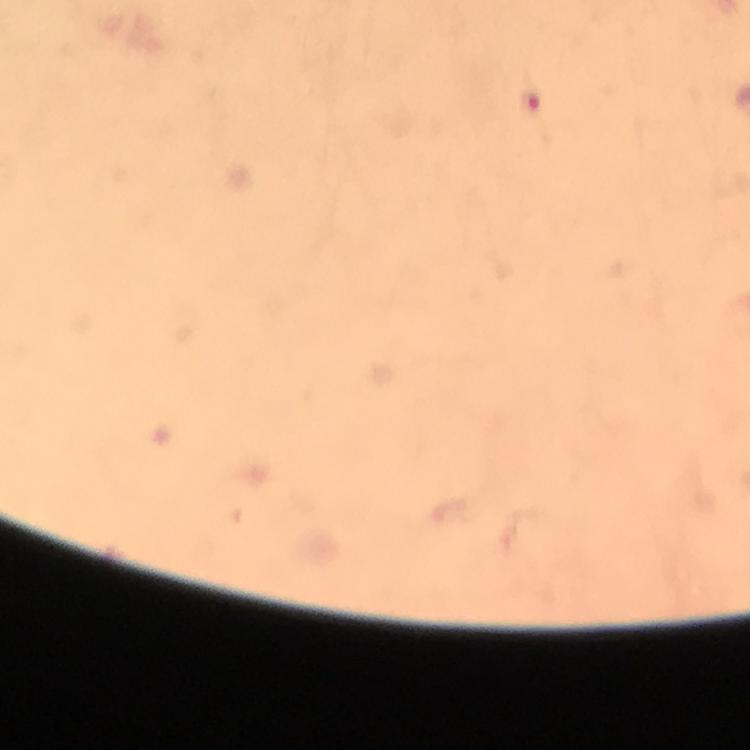

Approximate centers as (x, y) in pixels.
Summary:
  - Malaria parasite locations: (531, 107)
  - Capture: smartphone camera through the microscope
  - Image size: 750×750 pixels
  - Magnification: 100x
  - Preparation: thick blood film
  - Immersion oil: applied
  - Stain: Giemsa
  - Cropped from: one field of view
  - Context: from a diagnostic examination for malaria